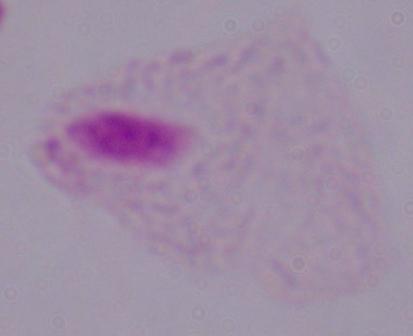 Photomicrograph. 1000x magnification. A trichomonad is seen.